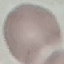

Summary:
  - Result: no malaria parasites seen
  - Image type: automatically extracted cell patch, resized to 64 × 64 pixels
  - Capture: smartphone through the microscope eyepiece
  - Preparation: thin blood film
  - Stain: Giemsa